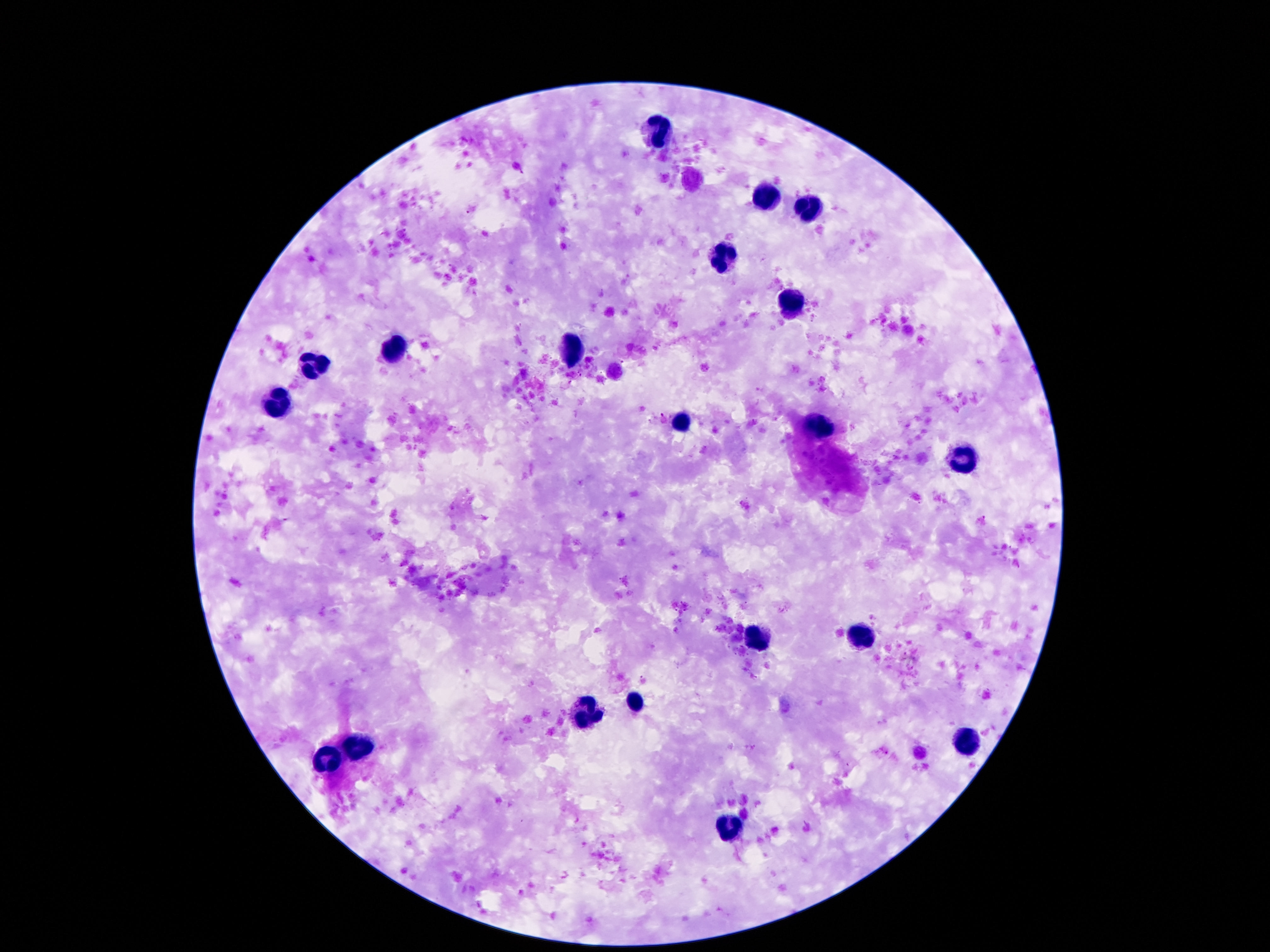

Approximate object centers, in pixels from the top-left corner. Leukocyte locations: (x=662, y=127), (x=765, y=195), (x=802, y=210), (x=720, y=262), (x=793, y=303), (x=570, y=348), (x=390, y=350), (x=306, y=363), (x=281, y=404), (x=679, y=422), (x=816, y=426), (x=959, y=460), (x=857, y=637), (x=756, y=641), (x=636, y=701), (x=580, y=714), (x=967, y=740), (x=361, y=748), (x=324, y=756), (x=734, y=829). Thick blood smear. Single field of view. 100x magnification. Image is 1270×952 pixels. Giemsa stain. Smartphone photograph taken through the microscope eyepiece. Patient malaria status: negative.